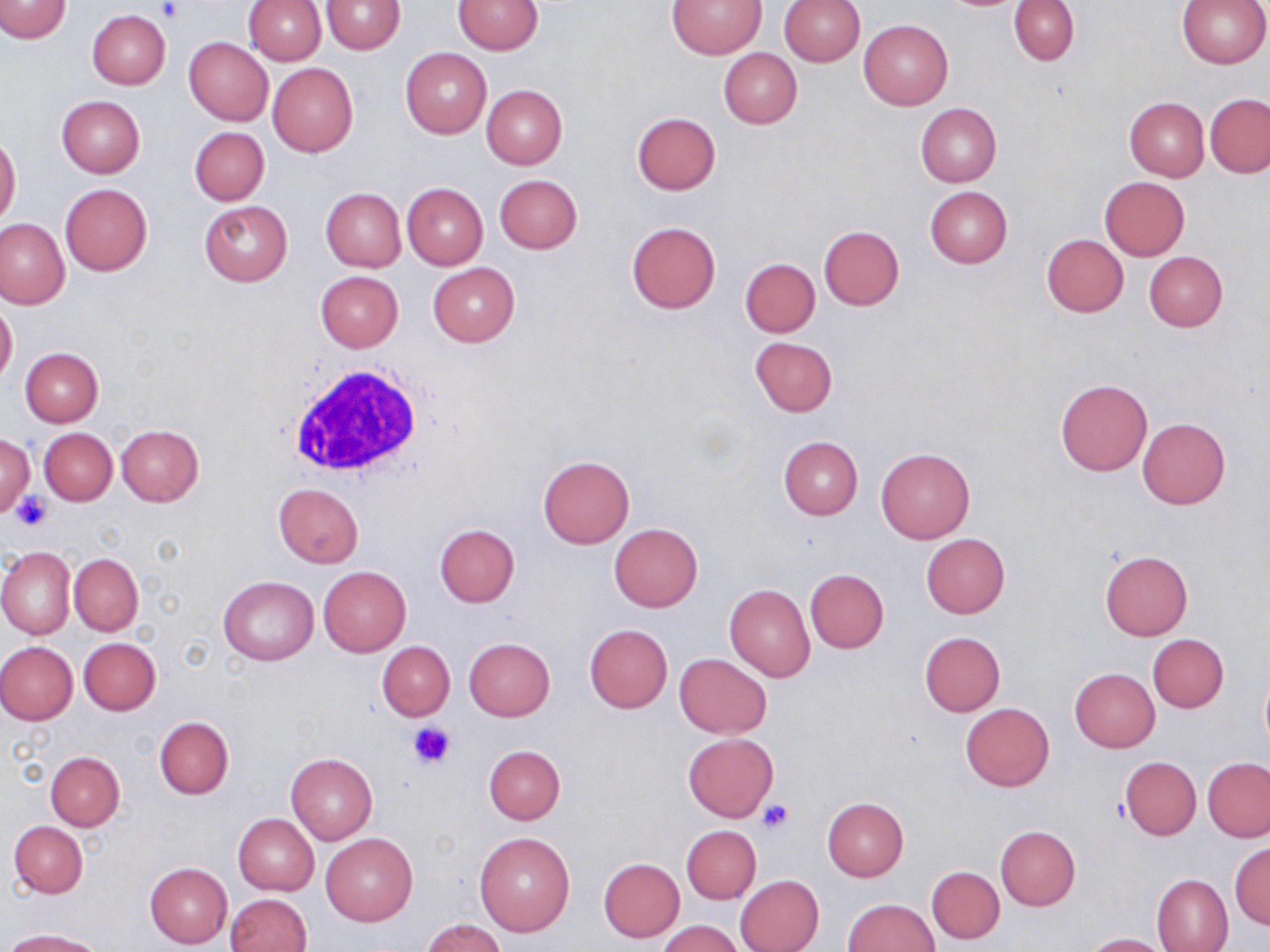
Approximate bounding boxes as [x1, y1, x2, y2] in pixels. Uninfected red blood cell locations: [1, 0, 70, 42], [243, 0, 327, 65], [321, 0, 404, 54], [454, 0, 543, 54], [669, 0, 765, 58], [779, 0, 864, 65], [1009, 0, 1079, 65], [1178, 0, 1270, 67], [87, 11, 170, 88], [859, 19, 953, 109], [183, 37, 273, 125], [401, 48, 491, 137], [718, 48, 801, 129], [268, 63, 358, 156], [482, 85, 567, 168], [1205, 93, 1270, 178], [55, 94, 145, 178], [1124, 97, 1209, 181], [915, 104, 1000, 188], [631, 112, 720, 195], [189, 125, 269, 205], [0, 131, 21, 228], [494, 175, 583, 255], [1100, 177, 1190, 260], [402, 182, 488, 269], [59, 183, 152, 276], [924, 186, 1013, 267], [321, 188, 405, 272], [199, 199, 292, 286], [0, 218, 69, 308], [626, 222, 720, 313], [819, 225, 904, 309], [1042, 234, 1128, 317], [1143, 251, 1228, 331], [740, 258, 821, 337], [428, 263, 518, 346], [315, 271, 403, 351], [0, 301, 18, 388], [750, 338, 837, 417], [21, 348, 103, 427], [1055, 379, 1153, 477], [1137, 418, 1230, 509], [116, 425, 204, 506], [39, 428, 117, 505], [0, 434, 35, 518], [778, 437, 863, 520], [875, 447, 974, 544], [537, 456, 634, 548], [275, 483, 363, 567], [609, 523, 702, 611], [435, 525, 520, 607], [921, 533, 1009, 619], [0, 547, 75, 640], [1100, 551, 1193, 640], [69, 553, 142, 635], [318, 566, 411, 657], [804, 569, 889, 653], [219, 575, 318, 665], [724, 585, 815, 682], [584, 624, 673, 713], [920, 631, 1005, 716], [1148, 634, 1228, 713], [78, 637, 160, 715], [464, 637, 554, 721], [377, 641, 455, 721], [0, 642, 78, 725], [674, 653, 771, 737], [1070, 668, 1159, 752], [1259, 671, 1270, 752], [960, 703, 1053, 790], [153, 716, 234, 799], [684, 733, 778, 820], [484, 746, 565, 824], [45, 751, 124, 830], [286, 752, 377, 844], [1120, 757, 1201, 840], [1203, 757, 1270, 842], [822, 797, 908, 881], [233, 813, 319, 895], [9, 821, 88, 897], [681, 824, 762, 904], [994, 825, 1080, 911], [474, 833, 575, 936], [321, 834, 416, 926], [1229, 844, 1270, 928], [598, 857, 685, 942], [145, 863, 232, 947], [927, 866, 1004, 944], [1152, 874, 1233, 952], [736, 875, 824, 952], [226, 894, 311, 952], [842, 898, 939, 952], [422, 918, 505, 952], [660, 920, 740, 952], [5, 929, 105, 951], [1085, 933, 1172, 952]. Platelet locations: [157, 2, 184, 23], [12, 491, 55, 531], [408, 720, 455, 769], [757, 799, 794, 834]. White blood cell locations: [283, 363, 430, 483]. Slide-level diagnosis: no evidence of blood parasites. Thin blood smear. Captured at 1000x magnification. Optical microscopy. May-Grünwald-Giemsa-stained preparation. Image is 1270×952 pixels. One field of a larger specimen.